Give the position of every Plasmodium parasite.
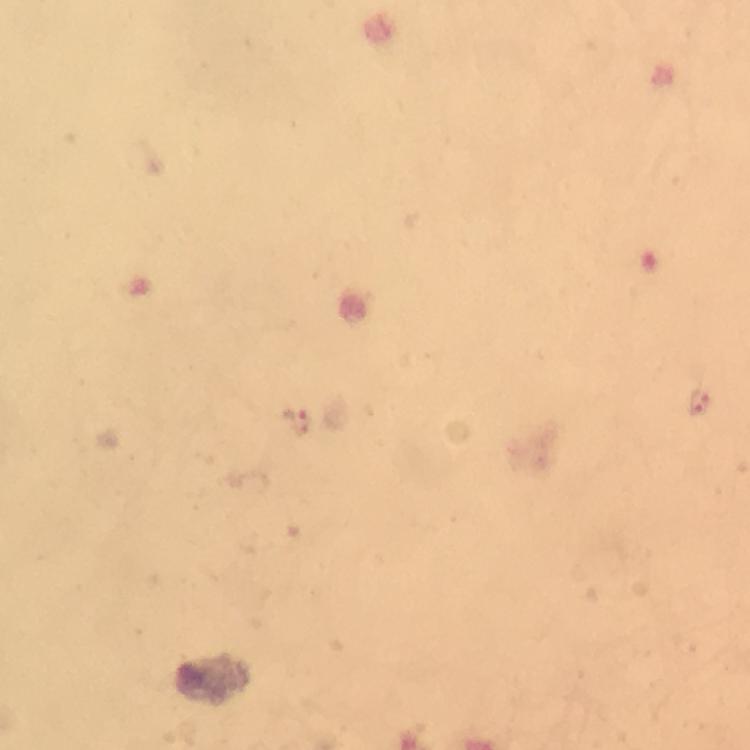
Approximate centers as {x, y} in pixels.
Plasmodium parasites: {700, 403}, {295, 423}.

A crop from one field of view. From a diagnostic examination for malaria. Image is 750×750 pixels. Giemsa-stained preparation. Immersion oil was used. Thick blood film. Photographed through the microscope with a smartphone camera. At 100x magnification.